Locate every uninfected red blood cell.
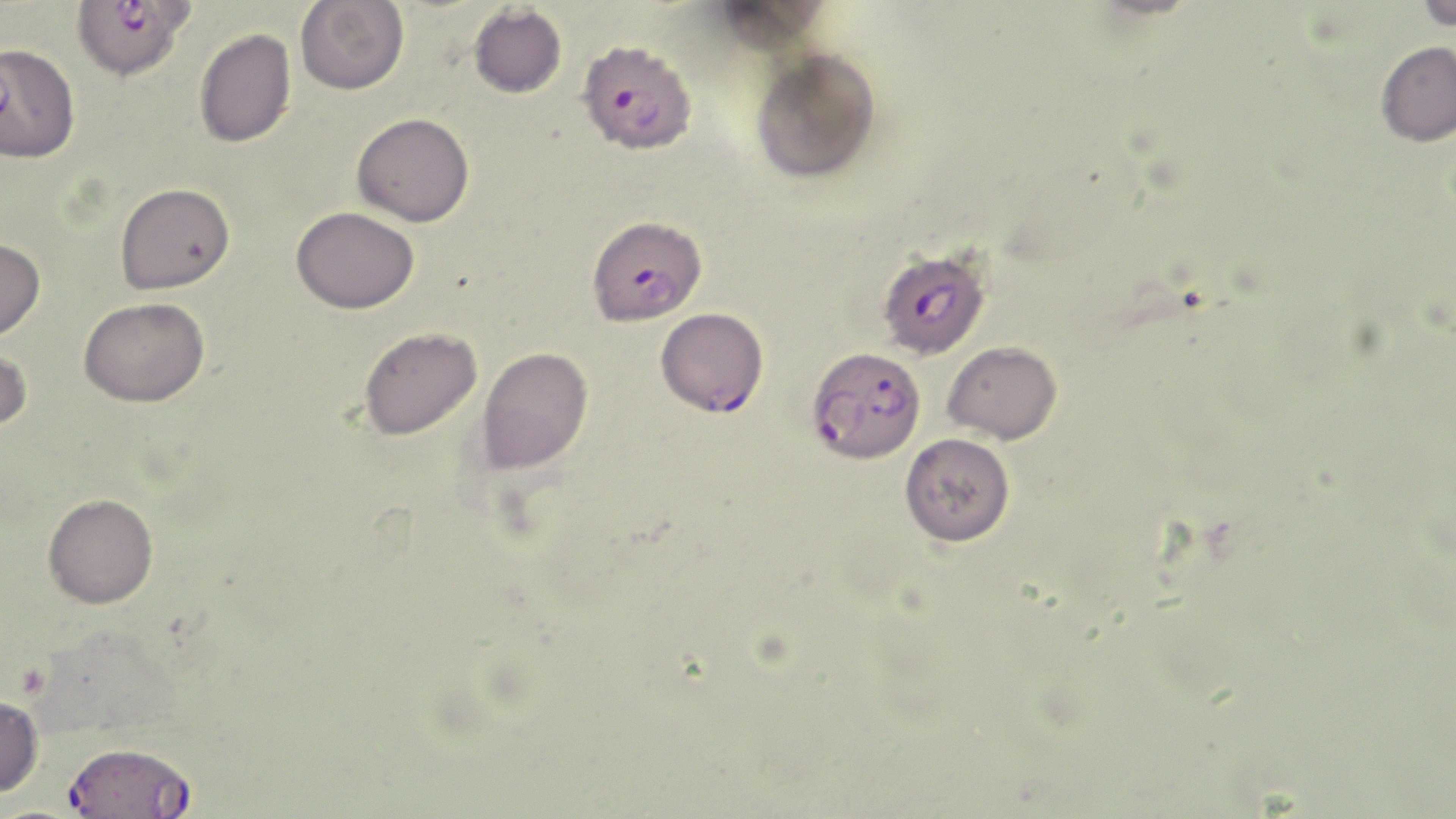

Approximate bounding boxes as named x1/y1/x2/y2 corners in pixels.
Uninfected red blood cells: (x1=706, y1=0, x2=832, y2=54), (x1=1415, y1=0, x2=1456, y2=31), (x1=295, y1=1, x2=409, y2=95), (x1=469, y1=4, x2=567, y2=98), (x1=194, y1=28, x2=297, y2=148), (x1=1376, y1=40, x2=1456, y2=146), (x1=750, y1=47, x2=880, y2=183), (x1=352, y1=112, x2=474, y2=227), (x1=115, y1=182, x2=235, y2=294), (x1=291, y1=206, x2=419, y2=313), (x1=0, y1=238, x2=45, y2=340), (x1=79, y1=296, x2=210, y2=406), (x1=359, y1=326, x2=482, y2=440), (x1=0, y1=341, x2=32, y2=433), (x1=943, y1=341, x2=1062, y2=444), (x1=477, y1=346, x2=593, y2=474), (x1=900, y1=433, x2=1015, y2=546), (x1=44, y1=493, x2=158, y2=608), (x1=0, y1=695, x2=44, y2=797).

Summary:
  - Plasmodium falciparum-infected red blood cell locations: (x1=74, y1=0, x2=196, y2=86), (x1=578, y1=39, x2=698, y2=161), (x1=587, y1=214, x2=706, y2=325), (x1=881, y1=251, x2=993, y2=364), (x1=657, y1=304, x2=767, y2=424), (x1=806, y1=346, x2=926, y2=463), (x1=64, y1=741, x2=197, y2=818)
  - Slide-level diagnosis: Plasmodium falciparum
  - Modality: optical microscopy
  - Image size: 1456×819 pixels
  - Field of view: one of a larger specimen
  - Preparation: thin blood smear
  - Stain: May-Grünwald-Giemsa
  - Magnification: 1000x